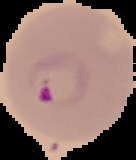
preparation = thin blood smear
result = malaria parasites identified
image type = cell region segmented out of the field of view; surrounding area masked to black
image size = 136×160 pixels